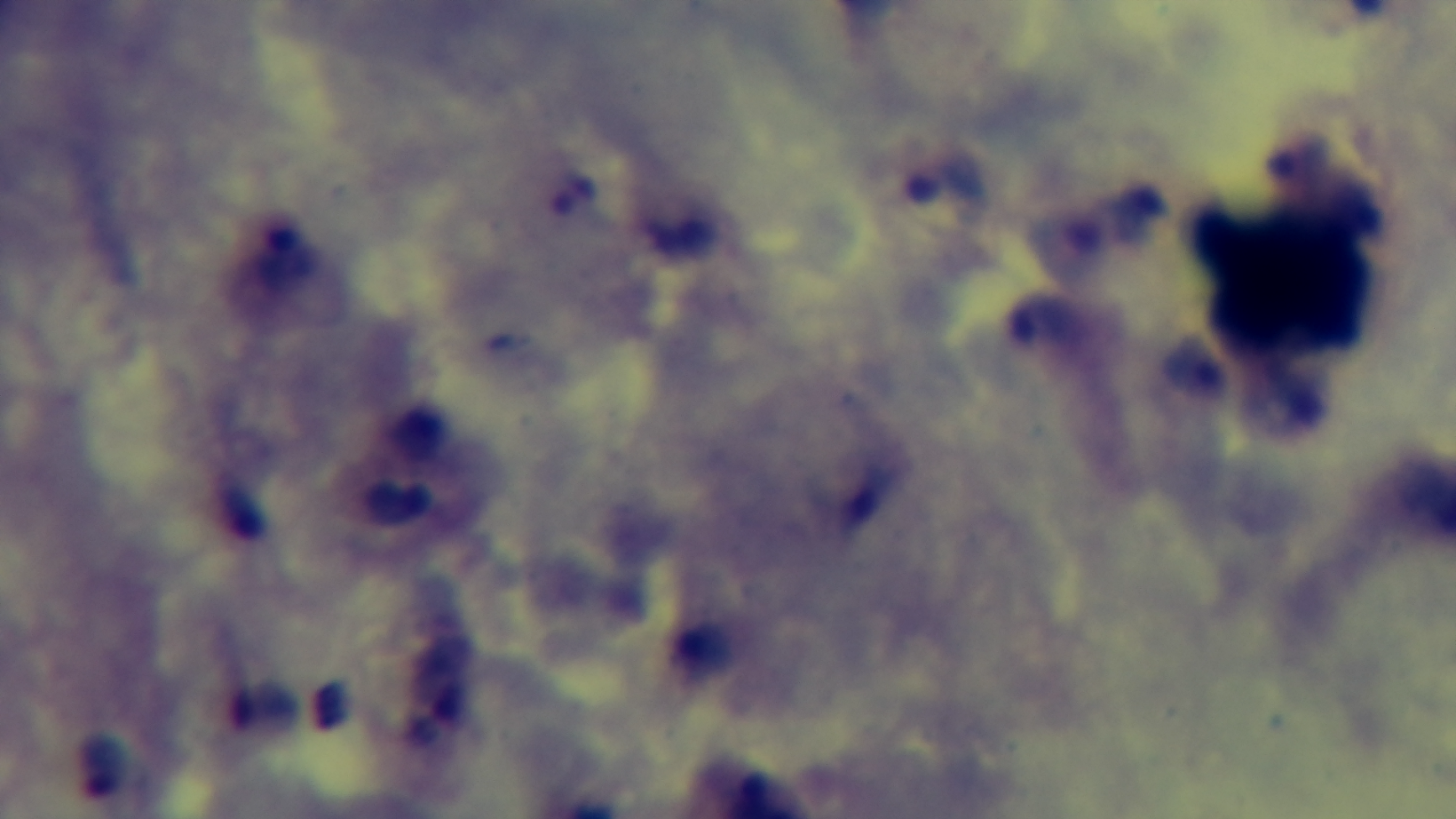

modality: light microscopy
field_of_view: single
capture: mounted 4K digital camera
stain: Giemsa
preparation: thick
malaria_status: infected
objective: 100x oil immersion